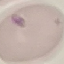

malaria_status: uninfected
image_type: automatically extracted cell patch, resized to 64 × 64 pixels
capture: smartphone camera at the microscope eyepiece
stain: Giemsa
preparation: thin blood smear